Classify this cell by malaria status.
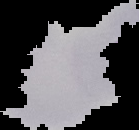

Parasitized.

Cell region segmented out of the field of view; the surrounding area is masked to black. Image is 139×130 pixels. From a thin blood film.